Report the malaria status of this cell.
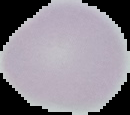

It is uninfected.

From a thin blood smear. Image is 130×115 pixels. Segmented cell region on a black background.